Assess this cell for malaria.
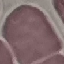

Uninfected.

Summary:
  - Capture: smartphone through the microscope eyepiece
  - Image type: automatically extracted cell patch, resized to 64 × 64 pixels
  - Preparation: thin blood smear
  - Stain: Giemsa